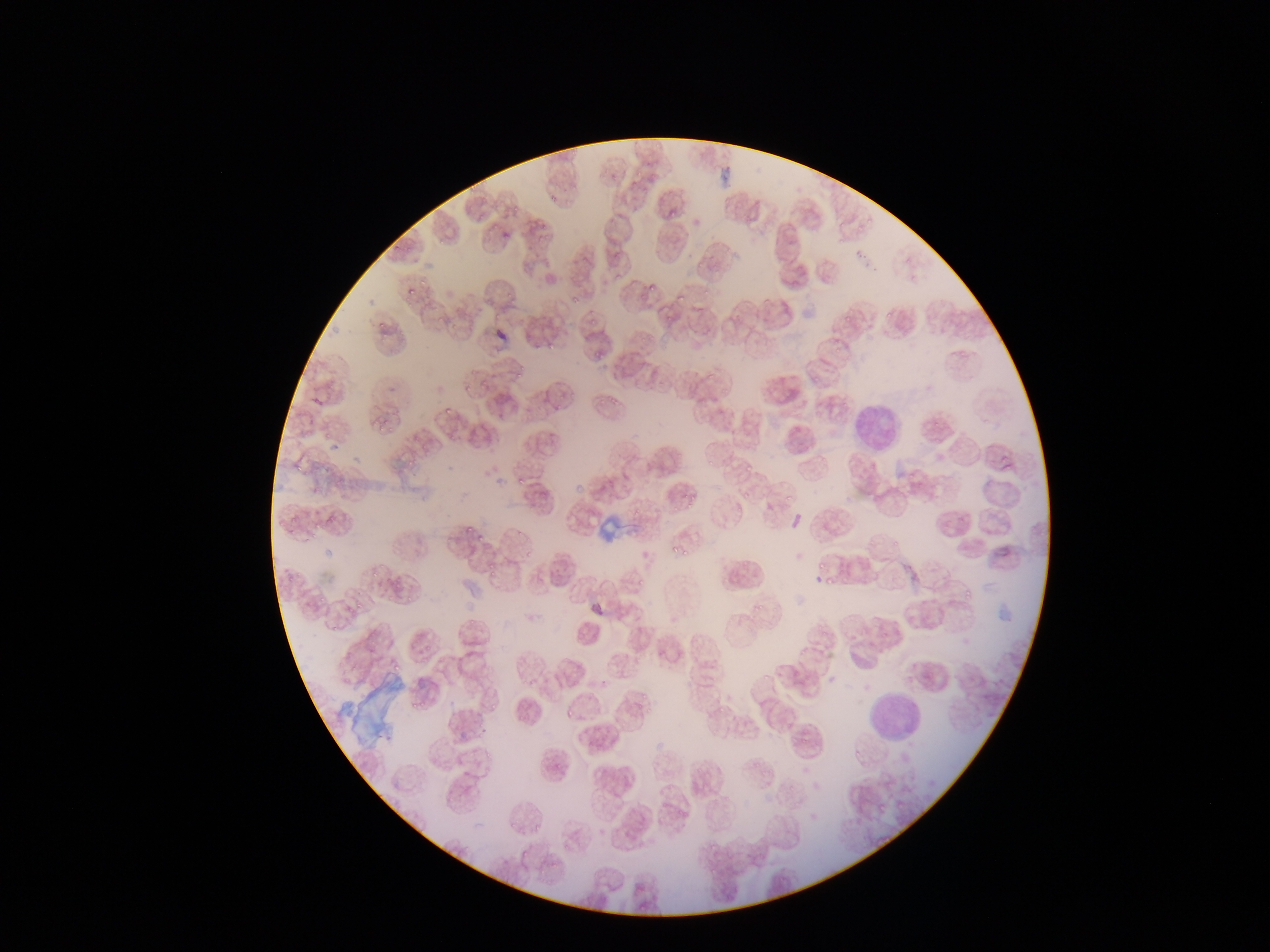

Approximate bounding boxes as (left, top, right, bottom) in pixels.
Summary:
  - Leukocyte locations: (840, 397, 901, 448), (863, 691, 927, 742)
  - Plasmodium parasite locations: (633, 169, 646, 178), (721, 170, 729, 182), (466, 182, 483, 197), (548, 195, 558, 204), (669, 203, 677, 226), (537, 220, 547, 228), (502, 231, 510, 240), (404, 246, 413, 253), (417, 278, 429, 292), (645, 279, 662, 293), (406, 287, 414, 295), (672, 290, 691, 306), (504, 293, 516, 300), (569, 293, 581, 308), (839, 307, 856, 325), (884, 308, 895, 319), (432, 314, 444, 325), (588, 315, 602, 327), (375, 320, 387, 332), (451, 325, 467, 333), (823, 340, 837, 348), (547, 341, 554, 349), (590, 351, 603, 361), (514, 365, 524, 380), (462, 372, 478, 383), (475, 380, 491, 397), (461, 385, 475, 394), (603, 393, 624, 405), (552, 403, 567, 413), (439, 409, 453, 421), (375, 418, 387, 432), (319, 428, 333, 446), (708, 453, 721, 470), (744, 457, 759, 472), (406, 458, 425, 471), (292, 460, 305, 477), (512, 474, 525, 485), (784, 484, 803, 503), (735, 485, 765, 508), (683, 493, 694, 510), (668, 498, 679, 516), (321, 511, 334, 530), (289, 513, 303, 526), (275, 520, 285, 530), (464, 523, 475, 535), (476, 531, 493, 543), (668, 541, 678, 556), (684, 547, 692, 560), (811, 558, 830, 571), (481, 567, 495, 580), (368, 570, 379, 583), (820, 574, 832, 591), (631, 578, 645, 591), (388, 580, 402, 594), (962, 588, 974, 601), (315, 590, 328, 607), (404, 595, 414, 606), (352, 596, 368, 614), (752, 601, 764, 617), (466, 616, 476, 627), (328, 620, 344, 636), (369, 639, 380, 648), (391, 659, 404, 672), (637, 689, 658, 706), (411, 694, 429, 714), (485, 698, 502, 713), (563, 708, 573, 718), (550, 757, 565, 779), (895, 800, 904, 808), (534, 822, 544, 830), (518, 849, 532, 861), (500, 856, 509, 866), (535, 865, 549, 878)
  - Artifact (stain precipitate or debris) locations: (598, 515, 627, 541), (346, 675, 406, 743)
  - Field of view: single
  - Image size: 1270×952 pixels
  - Preparation: thin blood smear
  - Country: Ghana
  - Capture: mobile-phone photograph through a microscope